Give the position of every malaria parasite.
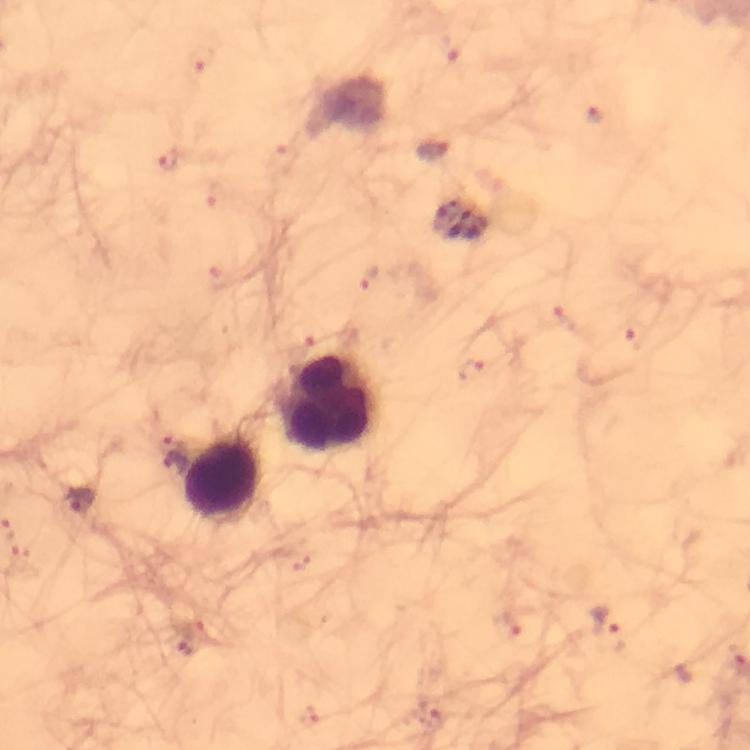

Approximate centers as [x, y] in pixels.
Malaria parasites: [434, 150], [174, 453], [79, 501], [607, 627].

Summary:
  - Leukocyte locations: [329, 404], [217, 476]
  - Capture: smartphone camera through the microscope
  - Context: from a diagnostic examination for malaria
  - Image size: 750×750 pixels
  - Preparation: thick blood film
  - Stain: Giemsa
  - Immersion oil: applied
  - Cropped from: a single field of view
  - Magnification: 100x